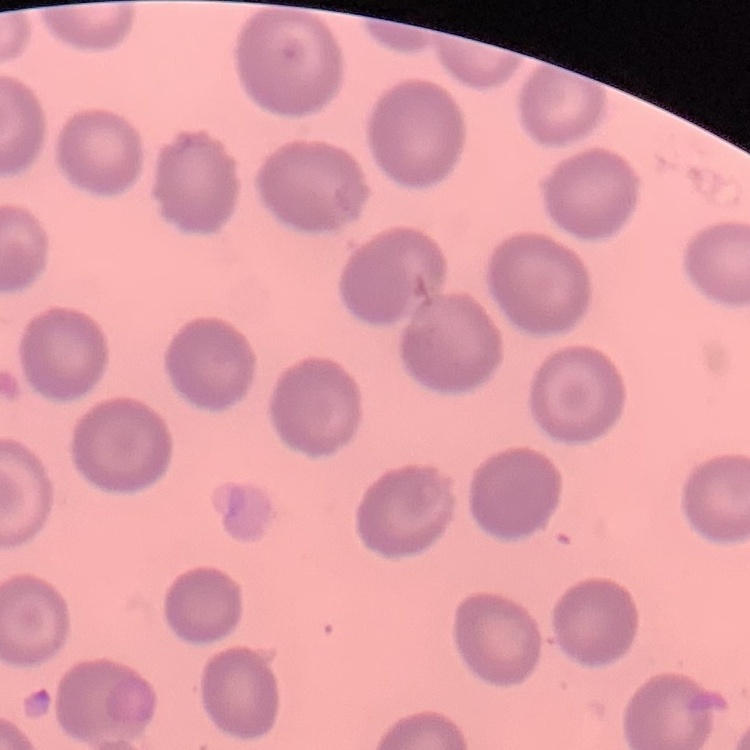
The red blood cells show no rouleaux formation. Stained with either Field's or Giemsa. Square crop of a larger photomicrograph. Thin blood film.